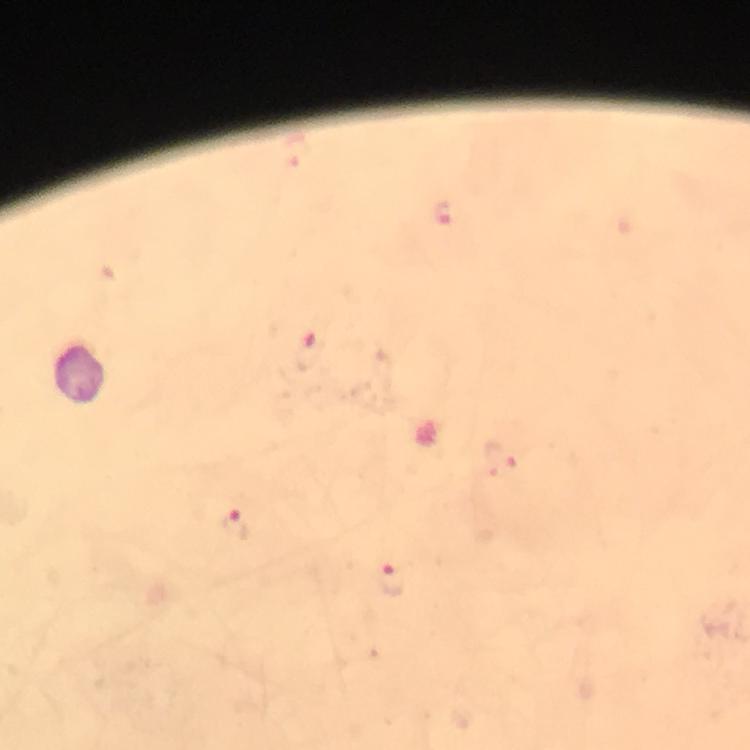
Approximate centers as [x, y] in pixels. Malaria parasite locations: [444, 214], [310, 353], [501, 458], [234, 525], [390, 582]. Giemsa stain. Immersion oil was used. Cropped region of a single field of view. 100x magnification. From a malaria diagnostic workup. Thick blood film. Image is 750×750 pixels. Smartphone photograph taken through a microscope.